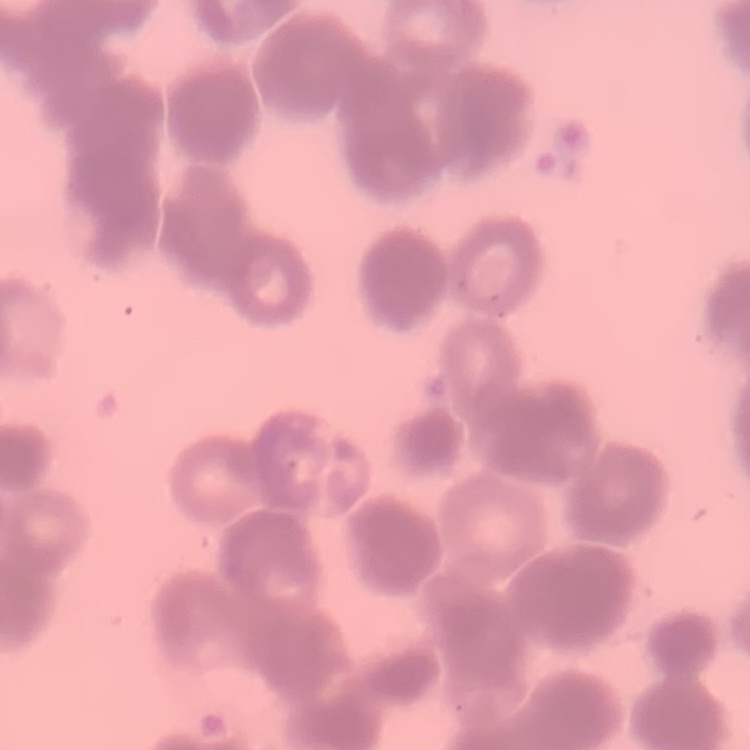

The red blood cells show rouleaux formation. Stained with either Field's or Giemsa. Square crop of a larger photomicrograph. Thin peripheral smear.